Assess this cell for malaria.
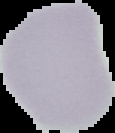
Uninfected.

Image is 115×133 pixels. From a thin blood smear. Segmented cell region on a black background.